Assess the morphology of the red blood cells.
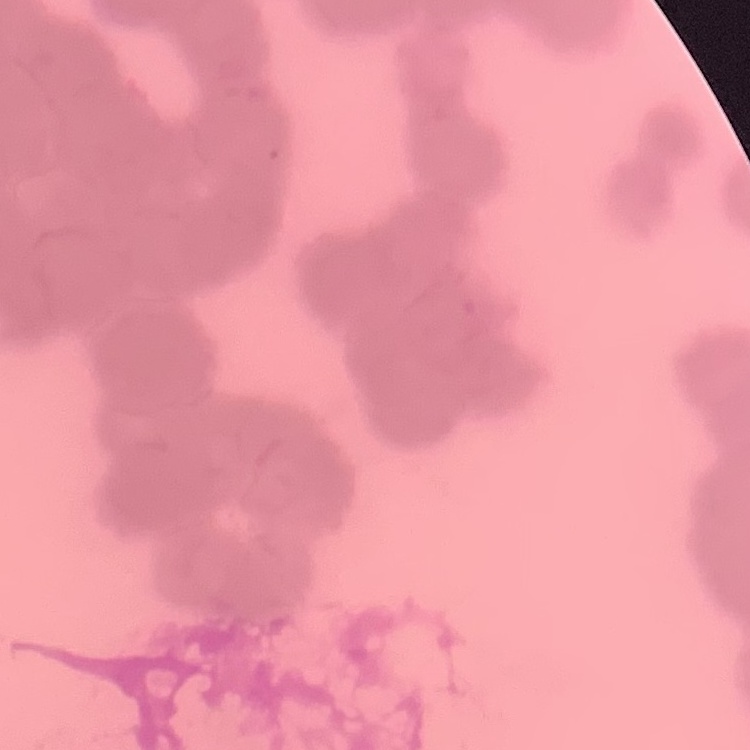
Rouleaux formation.

Summary:
  - Stain: Field's or Giemsa
  - Image type: square crop of a larger photomicrograph
  - Preparation: thin peripheral smear